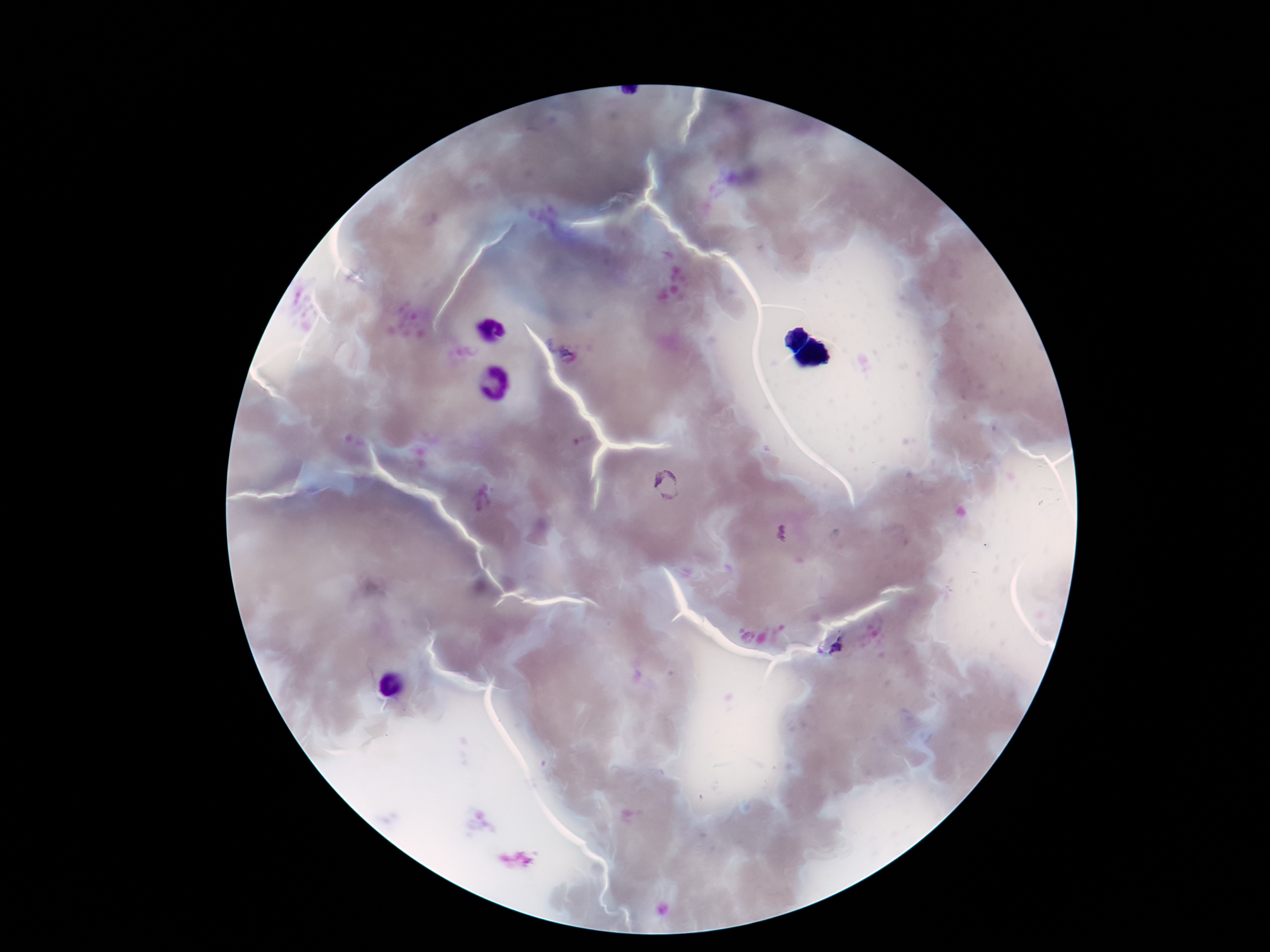
Approximate centers as {x, y} in pixels. Plasmodium parasite locations: {562, 345}, {666, 486}, {838, 649}. Smartphone photograph taken through the microscope eyepiece. Giemsa-stained preparation. Single field of view. Patient malaria status: infected. 100x magnification. Thick blood smear. Image is 1270×952 pixels.